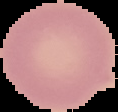

Summary:
  - Result: negative for malaria parasites
  - Image size: 118×112 pixels
  - Image type: segmented cell region on a black background
  - Preparation: thin blood smear